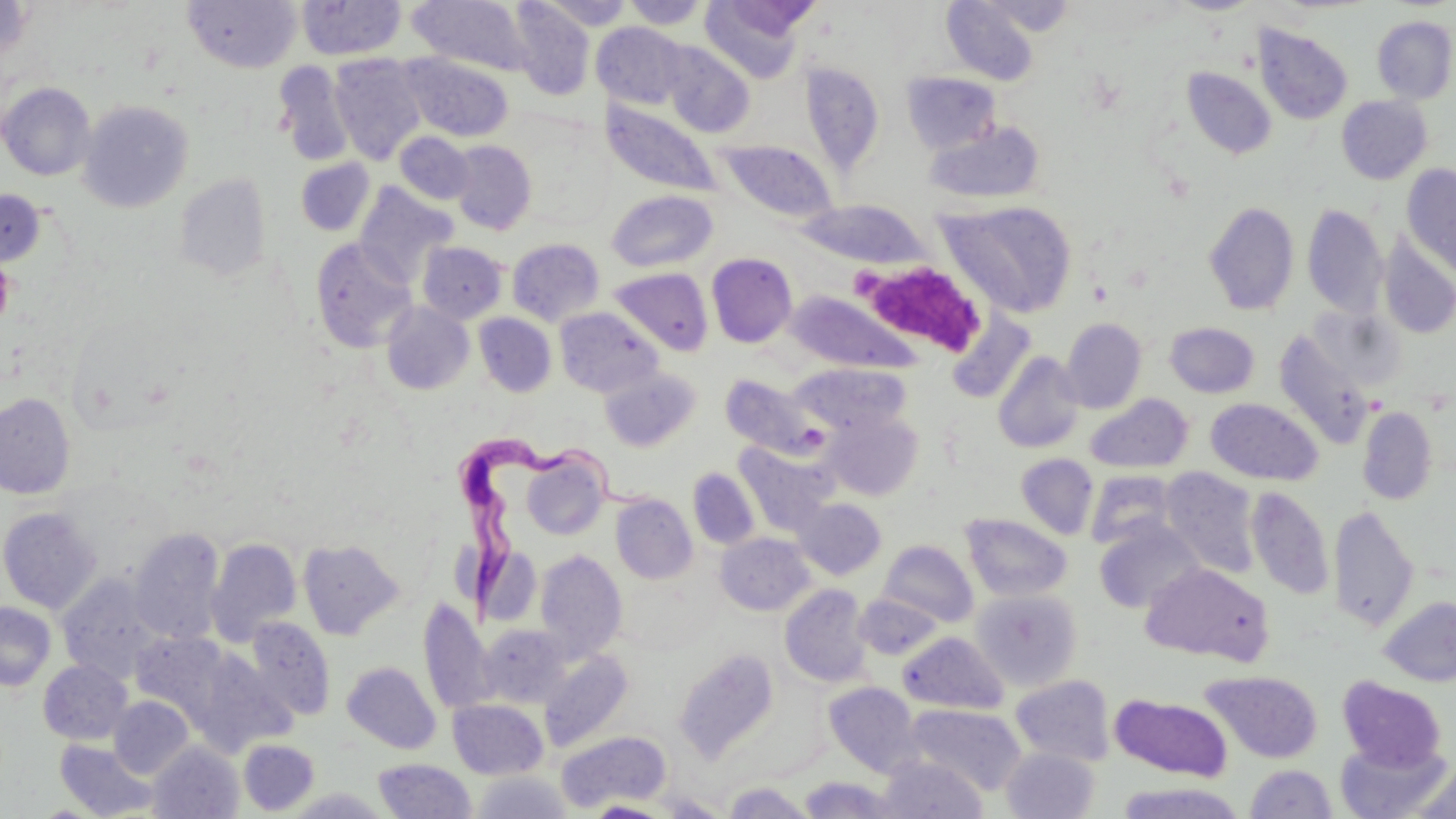
Trypanosoma brucei locations = approximate bounding boxes as named x1/y1/x2/y2 corners in pixels: (x1=450, y1=438, x2=654, y2=609)
slide-level diagnosis = Trypanosoma brucei
platelet locations = approximate bounding boxes as named x1/y1/x2/y2 corners in pixels: (x1=850, y1=266, x2=887, y2=294), (x1=878, y1=267, x2=983, y2=352)
magnification = 1000x
modality = optical microscopy
field of view = single
image size = 1456×819 pixels
stain = May-Grünwald-Giemsa
preparation = thin blood smear
uninfected red blood cell locations = approximate bounding boxes as named x1/y1/x2/y2 corners in pixels: (x1=700, y1=0, x2=814, y2=83), (x1=941, y1=0, x2=1041, y2=85), (x1=974, y1=0, x2=1077, y2=36), (x1=0, y1=1, x2=35, y2=62), (x1=183, y1=1, x2=301, y2=73), (x1=296, y1=1, x2=405, y2=60), (x1=406, y1=1, x2=536, y2=77), (x1=620, y1=1, x2=711, y2=29), (x1=508, y1=2, x2=595, y2=100), (x1=1372, y1=16, x2=1456, y2=104), (x1=592, y1=22, x2=688, y2=110), (x1=1252, y1=24, x2=1353, y2=125), (x1=662, y1=43, x2=755, y2=138), (x1=399, y1=52, x2=514, y2=142), (x1=329, y1=54, x2=427, y2=165), (x1=273, y1=61, x2=355, y2=166), (x1=799, y1=61, x2=886, y2=178), (x1=1182, y1=67, x2=1277, y2=159), (x1=901, y1=72, x2=1002, y2=154), (x1=0, y1=82, x2=96, y2=180), (x1=1337, y1=95, x2=1432, y2=184), (x1=602, y1=98, x2=722, y2=198), (x1=78, y1=99, x2=193, y2=213), (x1=923, y1=120, x2=1046, y2=205), (x1=396, y1=132, x2=474, y2=204), (x1=715, y1=139, x2=839, y2=224), (x1=450, y1=140, x2=537, y2=235), (x1=295, y1=158, x2=374, y2=236), (x1=1401, y1=164, x2=1456, y2=280), (x1=175, y1=173, x2=271, y2=281), (x1=354, y1=182, x2=456, y2=286), (x1=0, y1=189, x2=46, y2=266), (x1=606, y1=190, x2=718, y2=273), (x1=940, y1=199, x2=1078, y2=319), (x1=797, y1=200, x2=929, y2=269), (x1=1204, y1=201, x2=1299, y2=315), (x1=1302, y1=204, x2=1388, y2=318), (x1=1378, y1=236, x2=1456, y2=339), (x1=311, y1=238, x2=416, y2=353), (x1=507, y1=238, x2=605, y2=326), (x1=417, y1=241, x2=507, y2=324), (x1=706, y1=252, x2=797, y2=348), (x1=609, y1=267, x2=713, y2=356), (x1=785, y1=291, x2=925, y2=376), (x1=381, y1=302, x2=474, y2=394), (x1=1307, y1=305, x2=1405, y2=391), (x1=556, y1=307, x2=663, y2=397), (x1=474, y1=313, x2=556, y2=397), (x1=946, y1=315, x2=1037, y2=405), (x1=1060, y1=318, x2=1147, y2=413), (x1=1164, y1=322, x2=1260, y2=398), (x1=1273, y1=331, x2=1376, y2=449), (x1=993, y1=351, x2=1085, y2=453), (x1=791, y1=362, x2=910, y2=436), (x1=600, y1=367, x2=701, y2=452), (x1=720, y1=373, x2=827, y2=461), (x1=0, y1=392, x2=76, y2=499), (x1=1085, y1=394, x2=1193, y2=474), (x1=1205, y1=399, x2=1323, y2=485), (x1=1357, y1=405, x2=1437, y2=505), (x1=823, y1=412, x2=924, y2=500), (x1=733, y1=439, x2=839, y2=537), (x1=520, y1=450, x2=609, y2=541), (x1=1016, y1=453, x2=1099, y2=539), (x1=1161, y1=467, x2=1261, y2=578), (x1=687, y1=468, x2=760, y2=550), (x1=1085, y1=470, x2=1177, y2=549), (x1=1246, y1=486, x2=1334, y2=600), (x1=610, y1=493, x2=697, y2=584), (x1=794, y1=497, x2=886, y2=580), (x1=1328, y1=504, x2=1419, y2=631), (x1=0, y1=507, x2=102, y2=614), (x1=961, y1=514, x2=1072, y2=602), (x1=1093, y1=518, x2=1206, y2=614), (x1=129, y1=527, x2=225, y2=645), (x1=715, y1=533, x2=815, y2=615), (x1=206, y1=538, x2=302, y2=647), (x1=297, y1=538, x2=404, y2=639), (x1=878, y1=539, x2=979, y2=627), (x1=480, y1=547, x2=542, y2=628), (x1=534, y1=549, x2=627, y2=661), (x1=1140, y1=562, x2=1272, y2=664), (x1=57, y1=573, x2=164, y2=684), (x1=779, y1=584, x2=872, y2=687), (x1=971, y1=589, x2=1082, y2=691), (x1=855, y1=594, x2=944, y2=660), (x1=1378, y1=596, x2=1456, y2=686), (x1=418, y1=597, x2=496, y2=715), (x1=0, y1=602, x2=56, y2=691), (x1=244, y1=617, x2=335, y2=721), (x1=478, y1=624, x2=571, y2=708), (x1=898, y1=631, x2=1008, y2=714), (x1=130, y1=632, x2=229, y2=722), (x1=190, y1=647, x2=297, y2=755), (x1=674, y1=648, x2=780, y2=763), (x1=539, y1=649, x2=634, y2=753), (x1=38, y1=659, x2=133, y2=744), (x1=342, y1=661, x2=440, y2=754), (x1=1202, y1=670, x2=1322, y2=763), (x1=1011, y1=675, x2=1115, y2=766), (x1=1337, y1=676, x2=1448, y2=772), (x1=823, y1=681, x2=921, y2=776), (x1=1008, y1=681, x2=1232, y2=767), (x1=1110, y1=693, x2=1232, y2=781), (x1=109, y1=696, x2=193, y2=779), (x1=448, y1=699, x2=548, y2=779), (x1=903, y1=703, x2=1027, y2=796), (x1=557, y1=731, x2=670, y2=811), (x1=238, y1=739, x2=320, y2=815), (x1=1334, y1=739, x2=1452, y2=818), (x1=54, y1=740, x2=159, y2=818), (x1=148, y1=741, x2=243, y2=819), (x1=1002, y1=746, x2=1099, y2=819), (x1=879, y1=755, x2=987, y2=818), (x1=374, y1=759, x2=475, y2=819), (x1=1409, y1=762, x2=1456, y2=819), (x1=1245, y1=763, x2=1337, y2=818), (x1=473, y1=771, x2=570, y2=819), (x1=799, y1=777, x2=906, y2=818), (x1=1114, y1=781, x2=1246, y2=819), (x1=721, y1=783, x2=819, y2=818), (x1=285, y1=787, x2=392, y2=818), (x1=658, y1=793, x2=731, y2=817), (x1=586, y1=801, x2=671, y2=818)